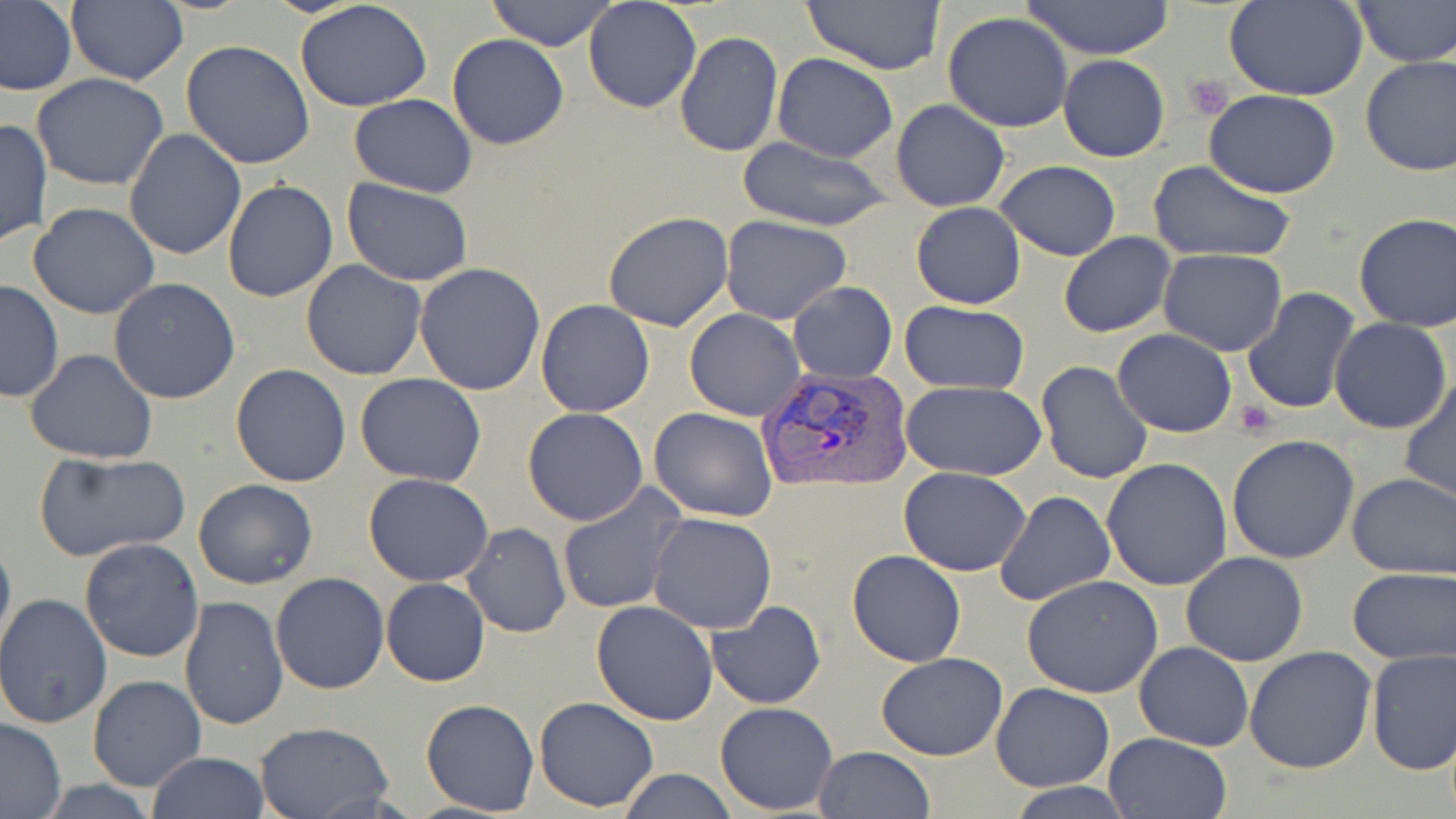
Approximate bounding boxes as named x1/y1/x2/y2 corners in pixels. Platelet locations: (x1=1185, y1=76, x2=1233, y2=120), (x1=1236, y1=402, x2=1275, y2=436). Plasmodium vivax-infected red blood cell locations: (x1=757, y1=365, x2=914, y2=496). Uninfected red blood cell locations: (x1=0, y1=0, x2=76, y2=97), (x1=294, y1=0, x2=433, y2=112), (x1=486, y1=0, x2=617, y2=51), (x1=583, y1=0, x2=702, y2=113), (x1=801, y1=0, x2=947, y2=75), (x1=1021, y1=0, x2=1176, y2=61), (x1=1351, y1=0, x2=1454, y2=67), (x1=1226, y1=1, x2=1367, y2=100), (x1=65, y1=2, x2=188, y2=86), (x1=943, y1=12, x2=1074, y2=132), (x1=673, y1=30, x2=784, y2=158), (x1=447, y1=34, x2=569, y2=150), (x1=181, y1=41, x2=315, y2=170), (x1=772, y1=53, x2=897, y2=161), (x1=1359, y1=54, x2=1456, y2=176), (x1=1058, y1=55, x2=1170, y2=162), (x1=30, y1=73, x2=170, y2=191), (x1=1205, y1=90, x2=1342, y2=198), (x1=347, y1=93, x2=477, y2=197), (x1=891, y1=99, x2=1010, y2=212), (x1=0, y1=119, x2=51, y2=248), (x1=123, y1=129, x2=247, y2=261), (x1=737, y1=136, x2=892, y2=234), (x1=996, y1=160, x2=1121, y2=261), (x1=1147, y1=160, x2=1299, y2=265), (x1=343, y1=179, x2=474, y2=288), (x1=221, y1=180, x2=340, y2=302), (x1=29, y1=202, x2=160, y2=319), (x1=910, y1=202, x2=1026, y2=310), (x1=603, y1=211, x2=733, y2=332), (x1=1354, y1=212, x2=1456, y2=331), (x1=721, y1=216, x2=851, y2=324), (x1=1059, y1=232, x2=1177, y2=338), (x1=1158, y1=249, x2=1286, y2=356), (x1=301, y1=260, x2=426, y2=380), (x1=415, y1=263, x2=548, y2=396), (x1=109, y1=278, x2=240, y2=405), (x1=0, y1=281, x2=64, y2=404), (x1=788, y1=283, x2=897, y2=384), (x1=1241, y1=288, x2=1363, y2=413), (x1=535, y1=300, x2=656, y2=417), (x1=901, y1=301, x2=1030, y2=394), (x1=685, y1=309, x2=806, y2=421), (x1=1331, y1=318, x2=1453, y2=435), (x1=1112, y1=329, x2=1236, y2=437), (x1=24, y1=349, x2=158, y2=464), (x1=1036, y1=360, x2=1153, y2=484), (x1=230, y1=364, x2=351, y2=487), (x1=355, y1=373, x2=486, y2=487), (x1=1399, y1=374, x2=1456, y2=503), (x1=899, y1=381, x2=1047, y2=481), (x1=648, y1=407, x2=779, y2=522), (x1=522, y1=408, x2=648, y2=526), (x1=1226, y1=434, x2=1360, y2=564), (x1=32, y1=449, x2=191, y2=564), (x1=1101, y1=457, x2=1233, y2=592), (x1=898, y1=467, x2=1031, y2=576), (x1=1346, y1=472, x2=1456, y2=579), (x1=364, y1=474, x2=494, y2=586), (x1=193, y1=478, x2=318, y2=590), (x1=556, y1=483, x2=688, y2=615), (x1=993, y1=490, x2=1115, y2=608), (x1=648, y1=512, x2=778, y2=635), (x1=462, y1=523, x2=571, y2=638), (x1=0, y1=529, x2=14, y2=661), (x1=77, y1=537, x2=203, y2=663), (x1=846, y1=549, x2=966, y2=667), (x1=1180, y1=551, x2=1309, y2=666), (x1=1347, y1=567, x2=1455, y2=664), (x1=270, y1=572, x2=390, y2=694), (x1=1022, y1=574, x2=1165, y2=698), (x1=381, y1=577, x2=490, y2=687), (x1=0, y1=595, x2=112, y2=729), (x1=179, y1=597, x2=288, y2=731), (x1=707, y1=600, x2=826, y2=709), (x1=590, y1=601, x2=719, y2=725), (x1=1134, y1=641, x2=1254, y2=750), (x1=1244, y1=646, x2=1377, y2=774), (x1=1364, y1=649, x2=1455, y2=775), (x1=876, y1=651, x2=1008, y2=759), (x1=87, y1=675, x2=207, y2=792), (x1=990, y1=682, x2=1114, y2=791), (x1=534, y1=696, x2=658, y2=811), (x1=421, y1=699, x2=540, y2=816), (x1=714, y1=702, x2=838, y2=814), (x1=0, y1=718, x2=67, y2=816), (x1=254, y1=721, x2=396, y2=819), (x1=1102, y1=731, x2=1233, y2=819), (x1=812, y1=747, x2=934, y2=819), (x1=146, y1=752, x2=271, y2=819), (x1=616, y1=769, x2=740, y2=818), (x1=28, y1=779, x2=167, y2=817), (x1=1005, y1=783, x2=1137, y2=817). Slide-level diagnosis: Plasmodium vivax. May-Grünwald-Giemsa-stained preparation. Optical microscopy. Thin blood film. One field of a larger specimen. 1000x magnification. Image is 1456×819 pixels.